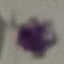

Result: negative for malaria parasites. Giemsa stain. Acquired by smartphone through the microscope eyepiece. Automatically extracted cell patch, resized to 64 × 64 pixels. Thin blood film.